Point out each leukocyte.
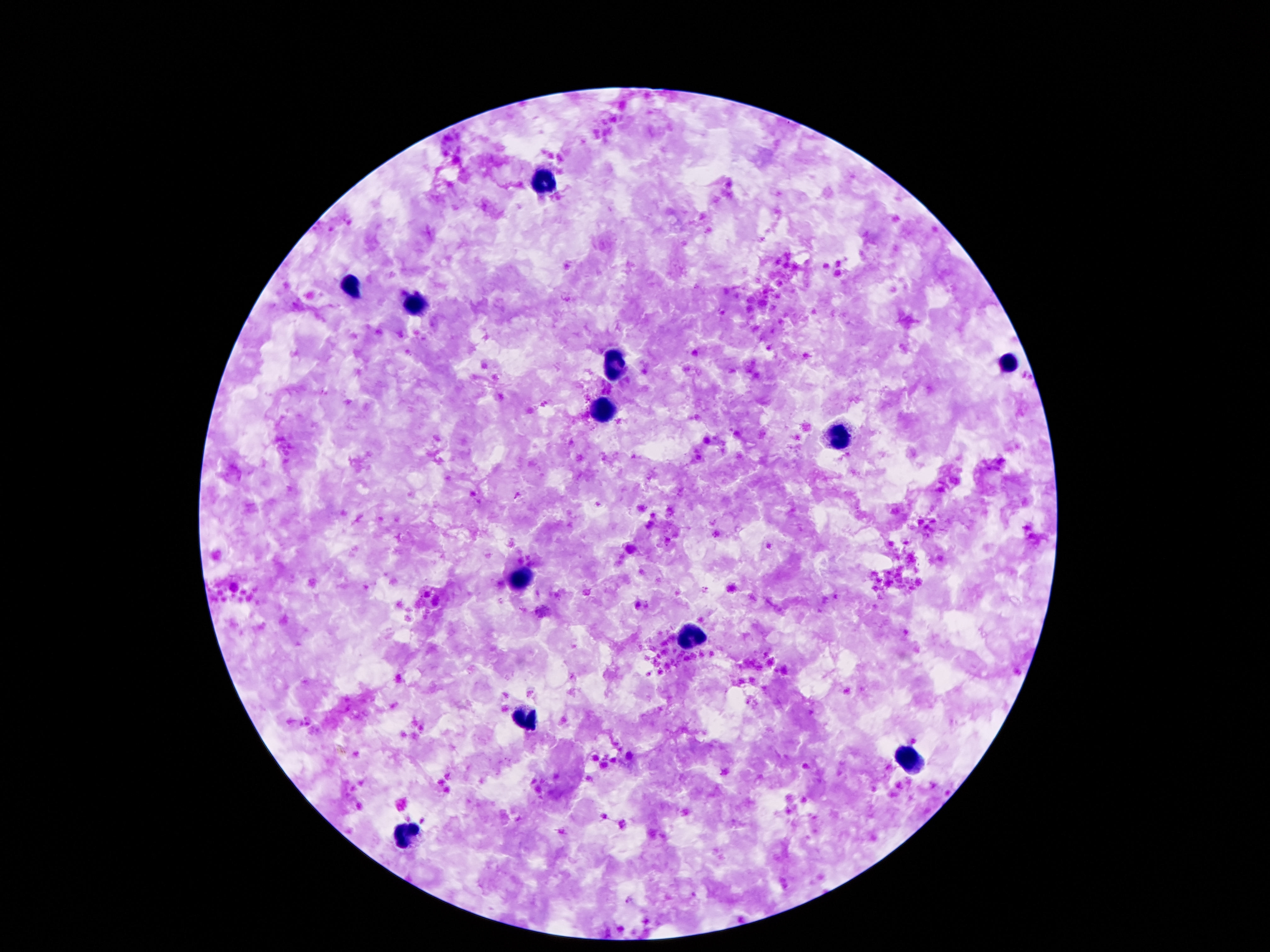
Approximate centers as [x, y] in pixels.
Leukocytes: [545, 182], [345, 288], [414, 306], [1006, 363], [617, 365], [603, 411], [840, 437], [523, 579], [691, 639], [525, 718], [910, 757], [404, 835].

Summary:
  - Capture: smartphone camera through the microscope eyepiece
  - Stain: Giemsa
  - Magnification: 100x
  - Field of view: one from this slide
  - Image size: 1270×952 pixels
  - Patient malaria status: uninfected
  - Preparation: thick blood smear